Locate every uninfected red blood cell.
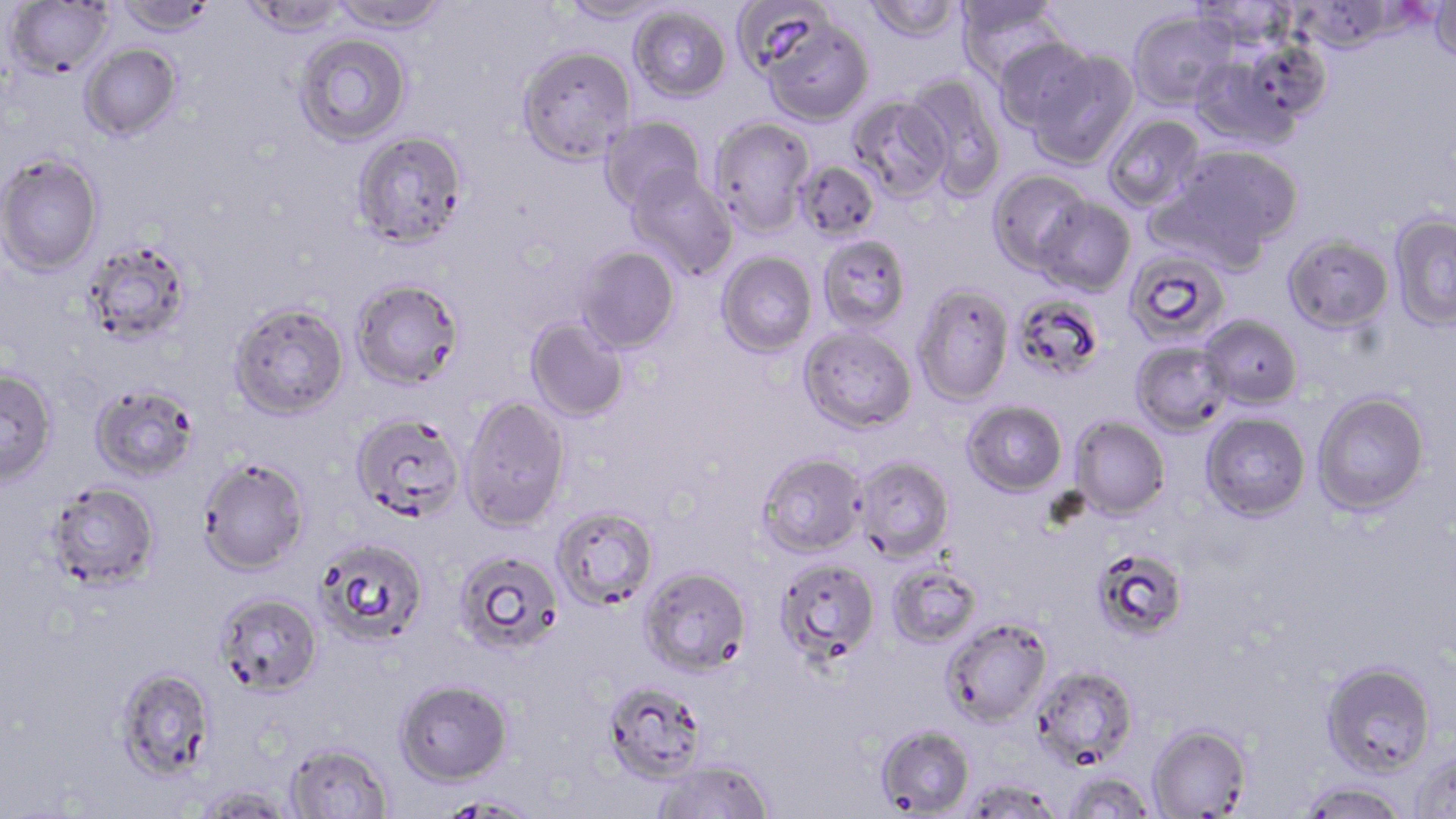

Approximate bounding boxes as named x1/y1/x2/y2 corners in pixels.
Uninfected red blood cells: (x1=114, y1=0, x2=219, y2=38), (x1=242, y1=0, x2=349, y2=39), (x1=329, y1=0, x2=451, y2=33), (x1=558, y1=0, x2=673, y2=25), (x1=732, y1=0, x2=835, y2=78), (x1=863, y1=0, x2=963, y2=44), (x1=1190, y1=0, x2=1299, y2=52), (x1=1292, y1=0, x2=1401, y2=55), (x1=5, y1=1, x2=115, y2=80), (x1=954, y1=1, x2=1065, y2=80), (x1=1429, y1=1, x2=1455, y2=65), (x1=629, y1=5, x2=731, y2=103), (x1=1128, y1=10, x2=1236, y2=110), (x1=761, y1=19, x2=873, y2=127), (x1=295, y1=33, x2=411, y2=146), (x1=992, y1=37, x2=1097, y2=133), (x1=80, y1=43, x2=182, y2=141), (x1=517, y1=46, x2=635, y2=164), (x1=1025, y1=49, x2=1139, y2=170), (x1=1189, y1=51, x2=1304, y2=150), (x1=905, y1=73, x2=1007, y2=199), (x1=849, y1=95, x2=952, y2=201), (x1=1103, y1=113, x2=1205, y2=213), (x1=599, y1=115, x2=707, y2=215), (x1=708, y1=116, x2=815, y2=237), (x1=351, y1=129, x2=468, y2=249), (x1=1170, y1=144, x2=1304, y2=256), (x1=0, y1=154, x2=104, y2=277), (x1=794, y1=160, x2=881, y2=242), (x1=625, y1=167, x2=738, y2=279), (x1=987, y1=168, x2=1093, y2=277), (x1=1034, y1=196, x2=1135, y2=297), (x1=1389, y1=212, x2=1456, y2=332), (x1=1283, y1=234, x2=1394, y2=335), (x1=817, y1=235, x2=911, y2=333), (x1=81, y1=241, x2=192, y2=348), (x1=574, y1=245, x2=680, y2=354), (x1=1124, y1=246, x2=1233, y2=349), (x1=716, y1=252, x2=817, y2=358), (x1=351, y1=280, x2=465, y2=391), (x1=913, y1=285, x2=1014, y2=405), (x1=1016, y1=298, x2=1105, y2=384), (x1=229, y1=304, x2=350, y2=423), (x1=1199, y1=314, x2=1302, y2=409), (x1=525, y1=317, x2=629, y2=423), (x1=798, y1=327, x2=917, y2=434), (x1=1131, y1=341, x2=1232, y2=436), (x1=0, y1=369, x2=59, y2=489), (x1=90, y1=386, x2=200, y2=483), (x1=1312, y1=391, x2=1430, y2=515), (x1=460, y1=396, x2=572, y2=533), (x1=962, y1=400, x2=1068, y2=496), (x1=1201, y1=412, x2=1311, y2=521), (x1=351, y1=414, x2=466, y2=525), (x1=1070, y1=416, x2=1171, y2=519), (x1=757, y1=453, x2=867, y2=558), (x1=853, y1=456, x2=954, y2=562), (x1=198, y1=459, x2=311, y2=577), (x1=45, y1=482, x2=161, y2=593), (x1=551, y1=506, x2=659, y2=610), (x1=316, y1=539, x2=429, y2=647), (x1=452, y1=548, x2=565, y2=656), (x1=1098, y1=557, x2=1185, y2=639), (x1=775, y1=558, x2=881, y2=664), (x1=887, y1=562, x2=983, y2=649), (x1=639, y1=567, x2=752, y2=676), (x1=214, y1=593, x2=323, y2=699), (x1=941, y1=617, x2=1054, y2=727), (x1=1321, y1=660, x2=1437, y2=777), (x1=1032, y1=665, x2=1139, y2=771), (x1=114, y1=667, x2=217, y2=782), (x1=394, y1=679, x2=513, y2=786), (x1=602, y1=680, x2=707, y2=785), (x1=1147, y1=723, x2=1252, y2=818), (x1=875, y1=724, x2=976, y2=818), (x1=284, y1=742, x2=394, y2=818), (x1=1411, y1=748, x2=1456, y2=818), (x1=652, y1=759, x2=774, y2=819), (x1=1064, y1=772, x2=1157, y2=818), (x1=961, y1=777, x2=1064, y2=819), (x1=1297, y1=780, x2=1410, y2=819), (x1=191, y1=787, x2=300, y2=818), (x1=438, y1=796, x2=539, y2=818).

{
  "slide_level_diagnosis": "Plasmodium falciparum",
  "field_of_view": "one of a larger specimen",
  "modality": "optical microscopy",
  "magnification": "1000x",
  "image_size": "1456×819 pixels",
  "stain": "May-Grünwald-Giemsa",
  "preparation": "thin blood smear"
}